Locate every P. falciparum parasite and identify its life-cycle stage.
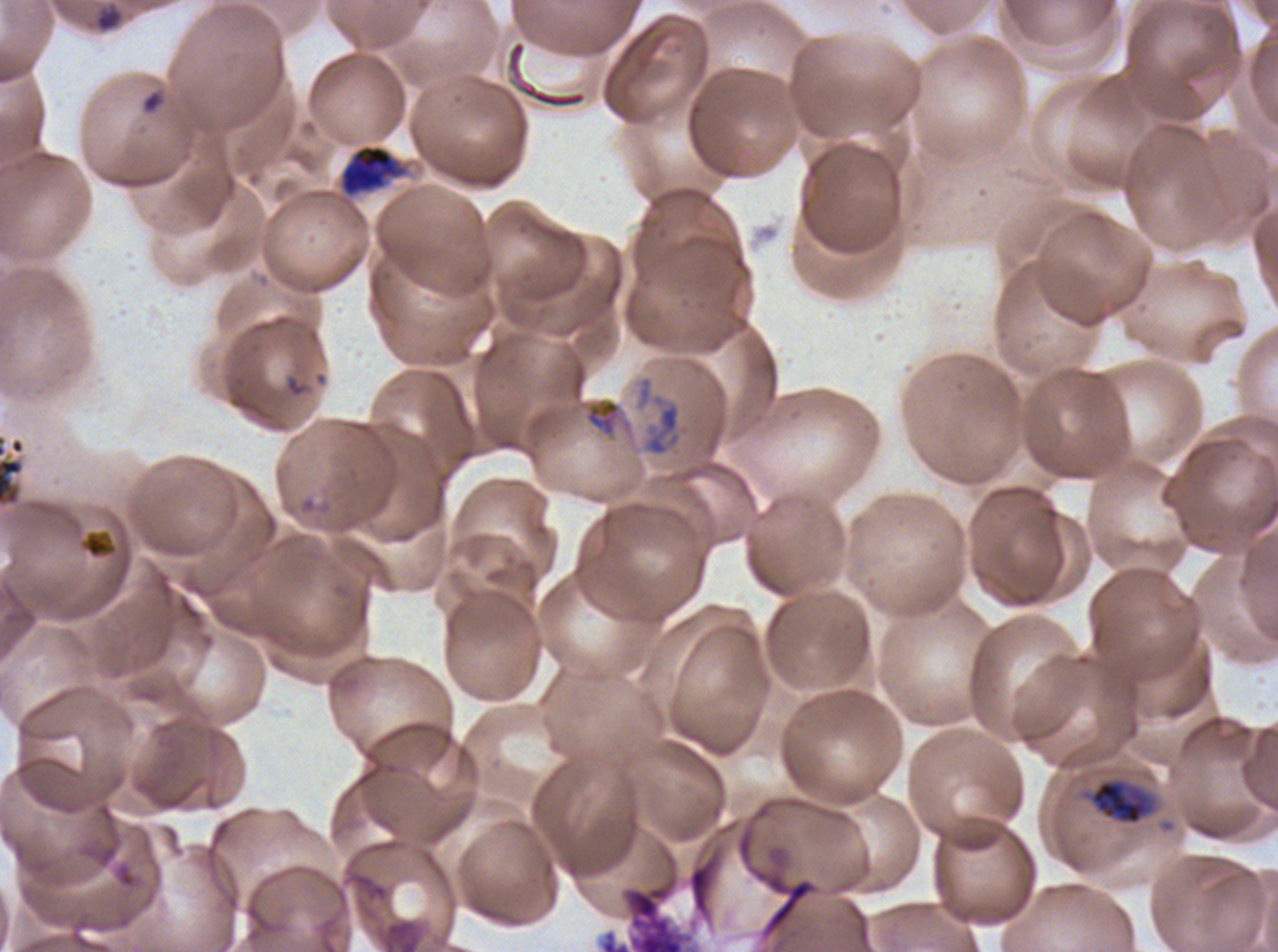
Approximate bounding rectangles given as corner coordinates in pixels from the top-left.
Rings: (x1=93, y1=3, x2=124, y2=33), (x1=141, y1=89, x2=166, y2=115), (x1=0, y1=433, x2=25, y2=508).
Late trophozoites: (x1=339, y1=144, x2=404, y2=197).
Early schizonts: (x1=1088, y1=776, x2=1158, y2=826).
No late-ring/early-trophozoite forms, mid trophozoites, late schizonts, segmenters, or gametocytes observed.

Debris locations: (x1=584, y1=397, x2=622, y2=437), (x1=80, y1=530, x2=117, y2=559). One sub-image of a larger composite. Giemsa stain. Life-cycle stages observed: ring, late trophozoite, early schizont. Ex-vivo P. falciparum culture from a patient in The Gambia, grown for 24 to 48 hours. Image is 1278×952 pixels. Thin blood smear.